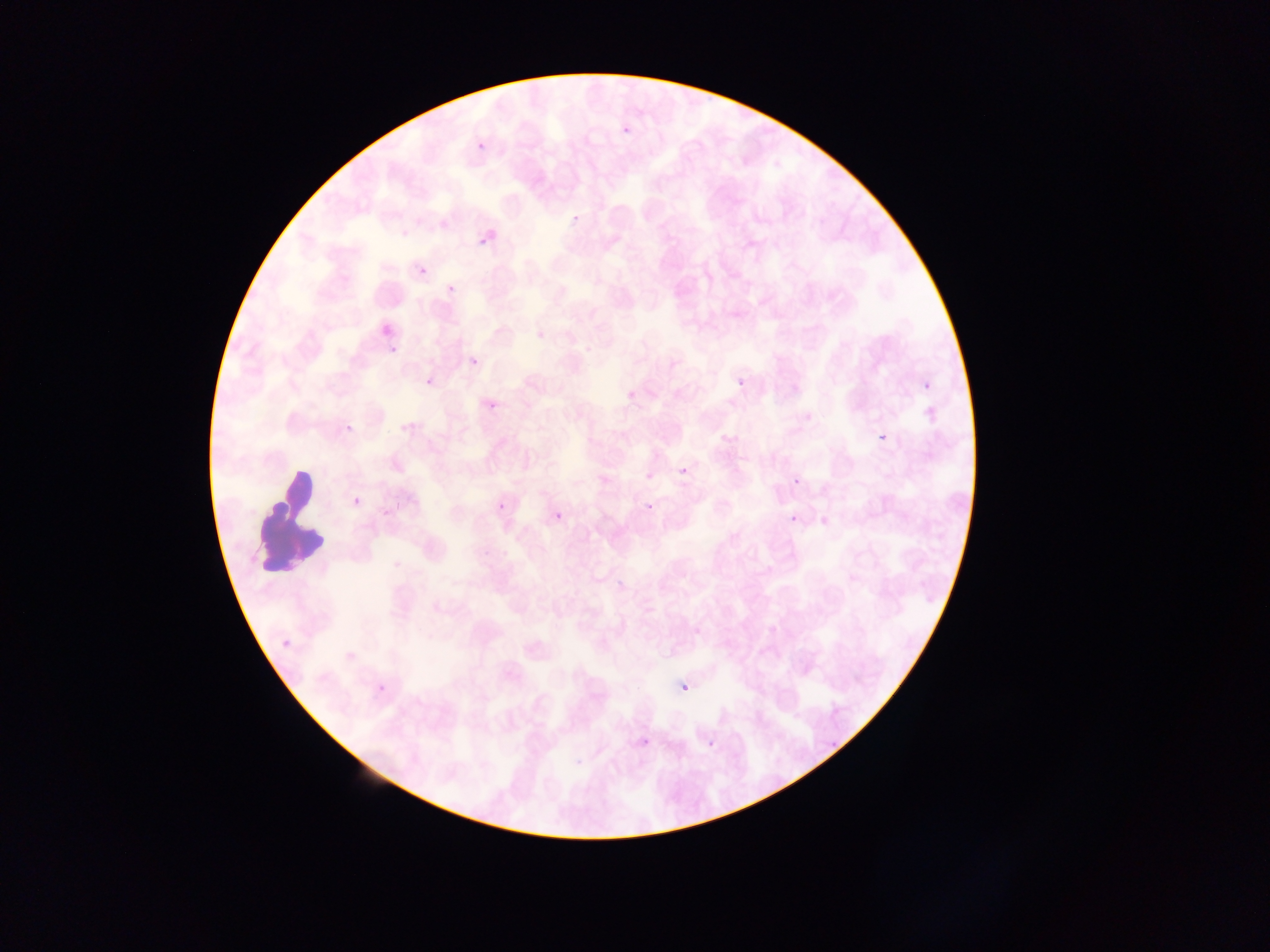

artifact (stain precipitate or debris) locations = approximate bounding boxes as (left, top, right, bottom) in pixels: (252, 470, 320, 580)
image size = 1270×952 pixels
country = Ghana
preparation = thin blood smear
field of view = single
malaria parasite locations = approximate bounding boxes as (left, top, right, bottom) in pixels: (620, 124, 633, 139), (476, 141, 486, 152), (564, 212, 580, 225), (439, 220, 448, 230), (476, 234, 486, 248), (418, 266, 428, 276), (446, 283, 456, 293), (388, 344, 399, 355), (468, 355, 480, 369), (425, 375, 435, 388), (734, 375, 751, 393), (918, 378, 935, 396), (625, 388, 637, 401), (487, 400, 499, 412), (343, 423, 349, 433), (875, 430, 891, 447), (675, 463, 693, 481), (788, 473, 807, 494), (350, 494, 365, 511), (495, 497, 512, 517), (644, 499, 655, 513), (553, 509, 569, 525), (786, 510, 806, 532), (555, 511, 565, 522), (278, 635, 295, 652), (375, 681, 391, 697), (681, 684, 690, 694)
capture = mobile-phone photograph through a microscope